Look for Plasmodium parasites.
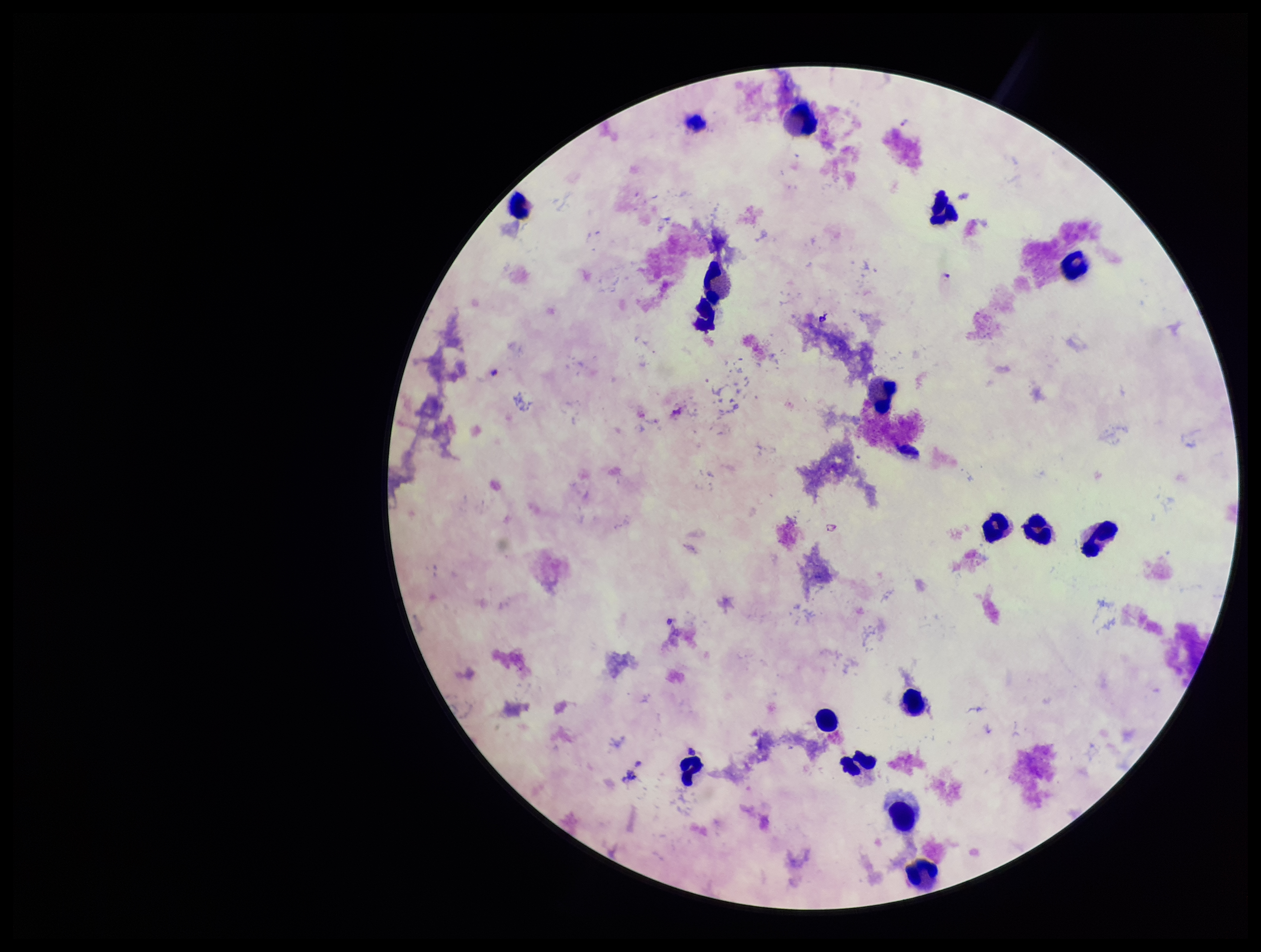

Detected.

leukocyte count = 16
image size = 1261×952 pixels
parasite count = 1
species reported for this patient = Plasmodium falciparum
patient malaria status = positive
stain = Giemsa
field of view = one from this slide
preparation = thick
capture = smartphone photograph through the microscope eyepiece